Classify this cell by malaria status.
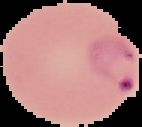
It is parasitized.

image type = cell region segmented out of the field of view; surrounding area masked to black
image size = 142×127 pixels
preparation = thin blood smear